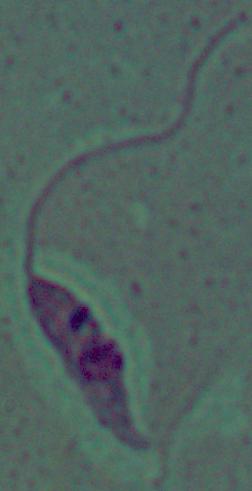

A Leishmania parasite is seen. Photomicrograph. 1000x magnification.